Point out each Plasmodium parasite and each leukocyte.
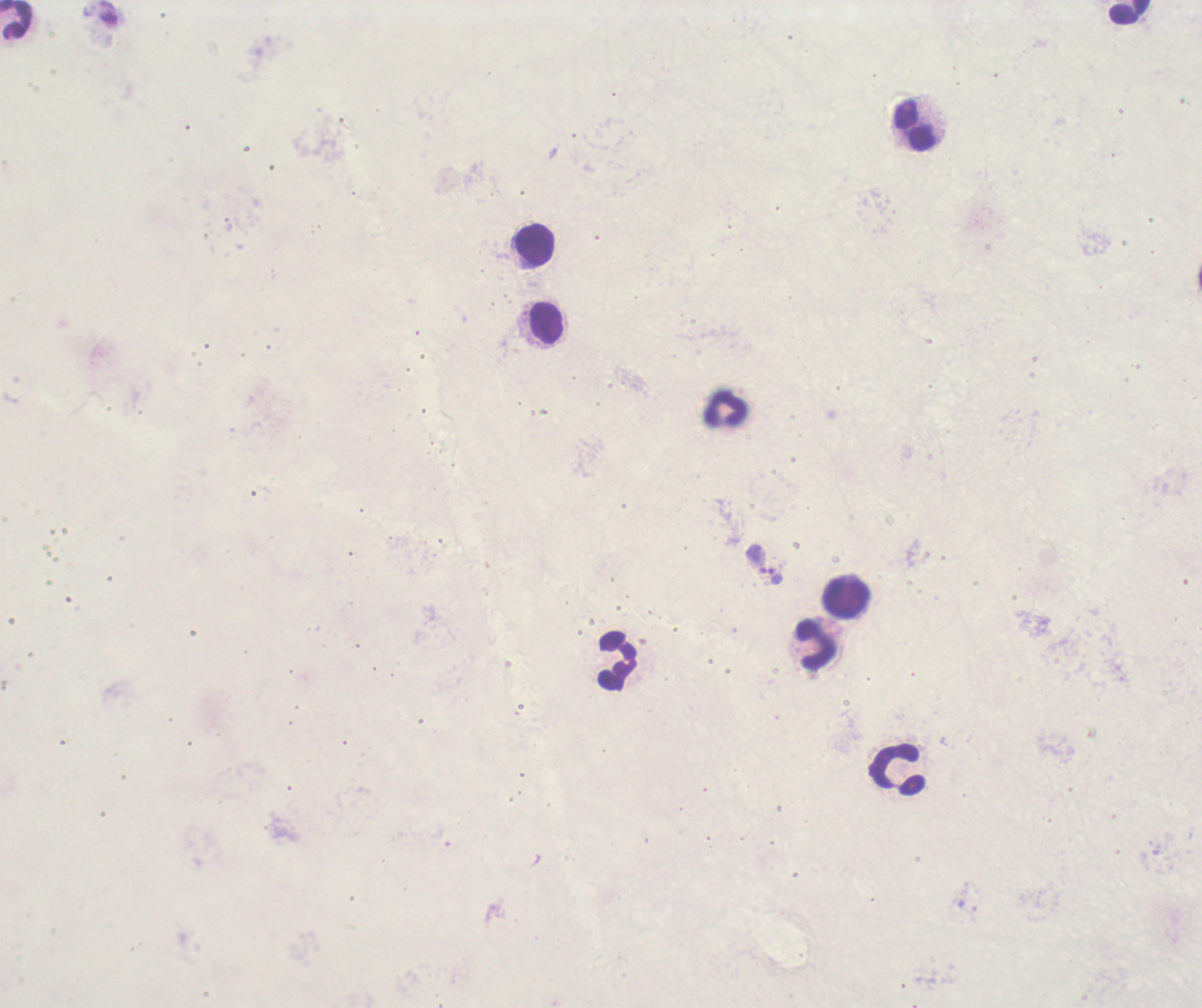

Approximate centers as {x, y} in pixels.
Trophozoites: {775, 576}.
No schizont or gametocyte forms observed.
Leukocytes: {1129, 12}, {17, 20}, {913, 127}, {533, 247}, {545, 324}, {726, 411}, {846, 596}, {814, 646}, {616, 662}, {899, 769}.

Romanowsky-stained preparation. Coloration quality: bad. Background quality: poor. Thick blood film. 100x magnification. One field from this slide. Previously used in a real diagnosis. Image is 1202×1008 pixels.